Name the blood parasite species.
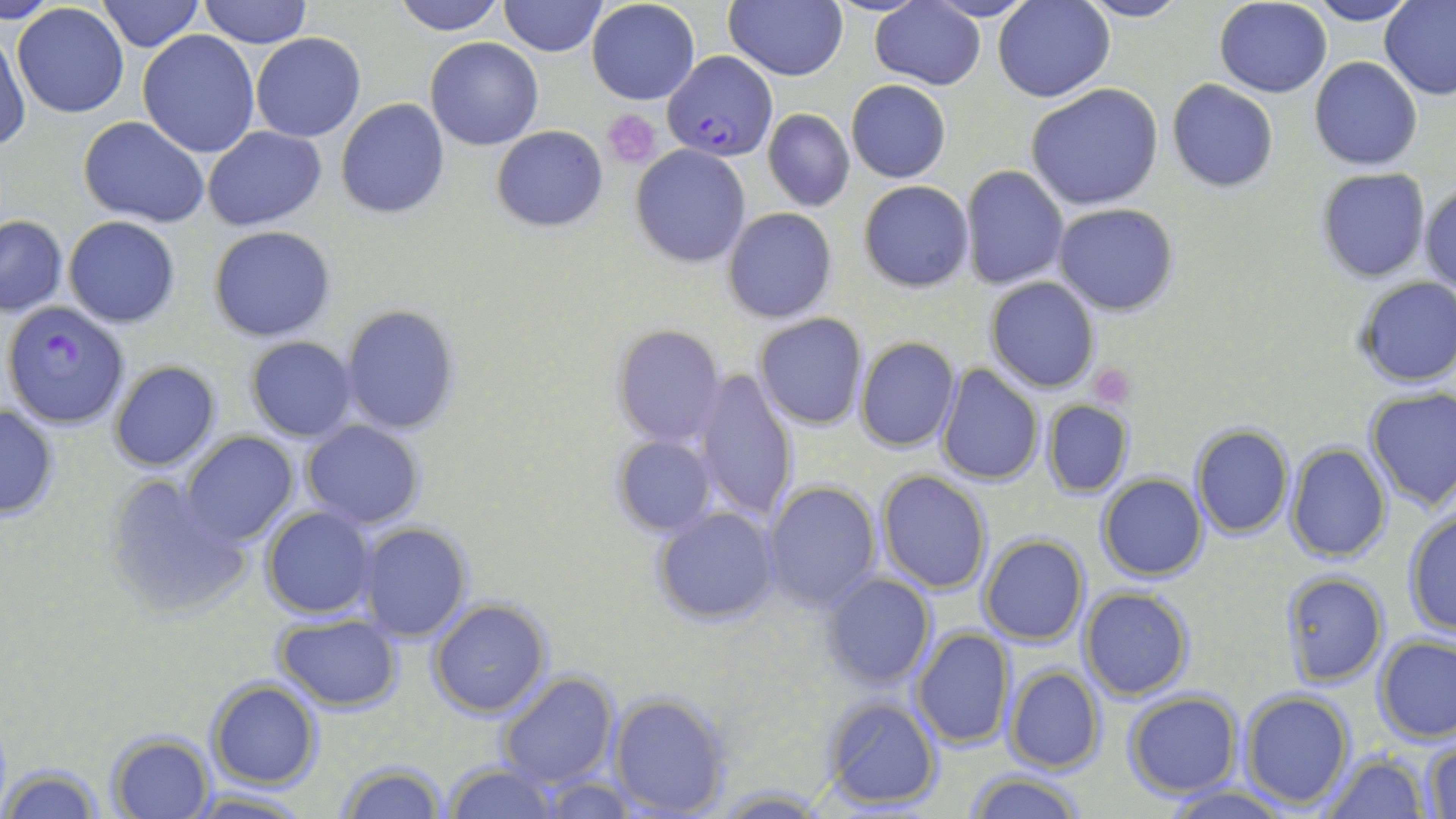

Plasmodium falciparum.

Summary:
  - Coordinate format: approximate bounding boxes as (x1, y1, x2, y2) in pixels
  - Platelet locations: (602, 110, 660, 167), (1089, 366, 1136, 409)
  - Uninfected red blood cell locations: (2, 0, 60, 21), (97, 0, 203, 50), (200, 0, 310, 48), (389, 0, 506, 35), (498, 0, 605, 56), (586, 0, 700, 105), (923, 0, 1039, 22), (992, 0, 1113, 102), (1303, 0, 1418, 25), (723, 1, 849, 81), (1076, 1, 1191, 24), (1213, 1, 1332, 97), (1378, 1, 1456, 100), (871, 2, 984, 89), (11, 4, 129, 118), (137, 30, 260, 157), (0, 32, 27, 151), (251, 32, 366, 142), (425, 38, 543, 151), (1308, 56, 1423, 171), (846, 81, 951, 183), (1167, 81, 1278, 192), (1025, 83, 1165, 211), (337, 99, 450, 220), (763, 108, 855, 212), (78, 116, 210, 229), (203, 126, 327, 230), (492, 126, 607, 231), (630, 145, 751, 268), (961, 165, 1069, 290), (1314, 166, 1431, 283), (859, 179, 974, 293), (1420, 182, 1455, 298), (1055, 203, 1177, 315), (722, 206, 837, 323), (62, 215, 181, 328), (0, 216, 67, 316), (209, 226, 335, 342), (729, 230, 845, 394), (1353, 277, 1455, 387), (986, 278, 1100, 393), (337, 305, 462, 437), (752, 313, 868, 429), (613, 323, 726, 447), (244, 337, 359, 442), (856, 337, 960, 452), (108, 361, 221, 472), (936, 365, 1043, 483), (693, 370, 797, 522), (1363, 388, 1456, 512), (1041, 400, 1133, 498), (0, 403, 59, 520), (300, 422, 424, 529), (1191, 424, 1294, 538), (182, 433, 299, 546), (612, 434, 717, 535), (1286, 442, 1392, 564), (876, 470, 992, 594), (102, 472, 251, 620), (1095, 474, 1208, 582), (763, 481, 883, 610), (260, 505, 377, 619), (650, 506, 782, 627), (1401, 509, 1455, 635), (358, 524, 472, 643), (978, 534, 1089, 645), (1281, 570, 1388, 686), (820, 572, 936, 689), (1078, 587, 1193, 699), (428, 600, 551, 717), (274, 613, 403, 709), (910, 628, 1013, 749), (1375, 635, 1456, 743), (1002, 665, 1106, 774), (497, 671, 619, 789), (206, 680, 322, 788), (1238, 690, 1355, 809), (606, 691, 731, 817), (1122, 692, 1241, 798), (820, 697, 942, 808), (107, 731, 214, 817), (1423, 741, 1455, 819), (1324, 753, 1428, 819), (335, 760, 448, 818), (3, 762, 105, 819), (440, 763, 561, 818), (963, 772, 1088, 819), (534, 775, 639, 816), (1160, 785, 1293, 818), (704, 786, 834, 816), (185, 789, 312, 818)
  - Plasmodium falciparum-infected red blood cell locations: (664, 51, 778, 160), (4, 300, 130, 428)
  - Stain: May-Grünwald-Giemsa
  - Image size: 1456×819 pixels
  - Preparation: thin blood film
  - Magnification: 1000x
  - Modality: optical microscopy
  - Field of view: single